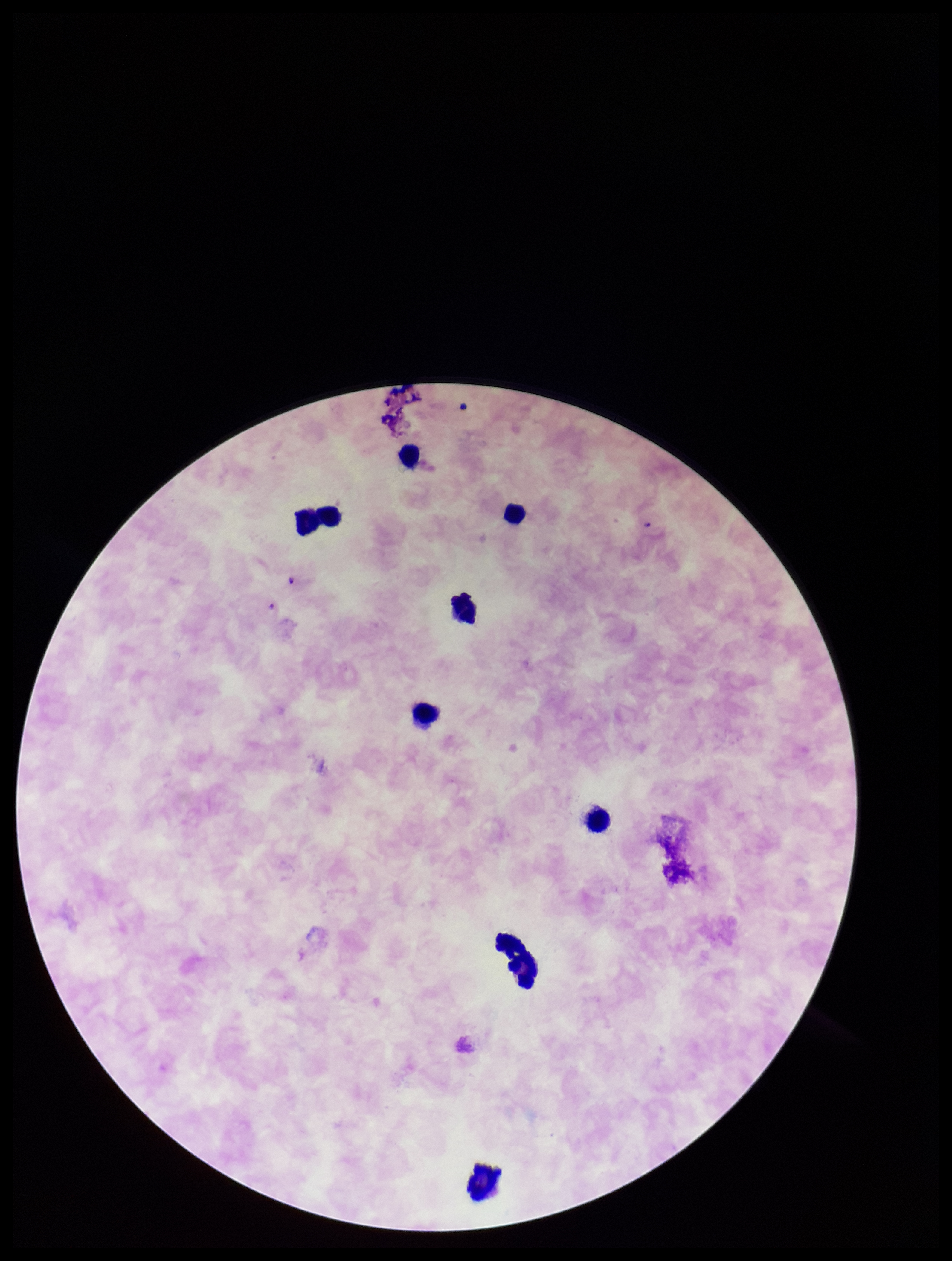
field of view = single
parasite count = 0
leukocyte count = 8
capture = smartphone photograph through the microscope eyepiece
Plasmodium parasites = none identified
species reported for this patient = Plasmodium falciparum
patient malaria status = positive
image size = 952×1261 pixels
preparation = thick
stain = Giemsa